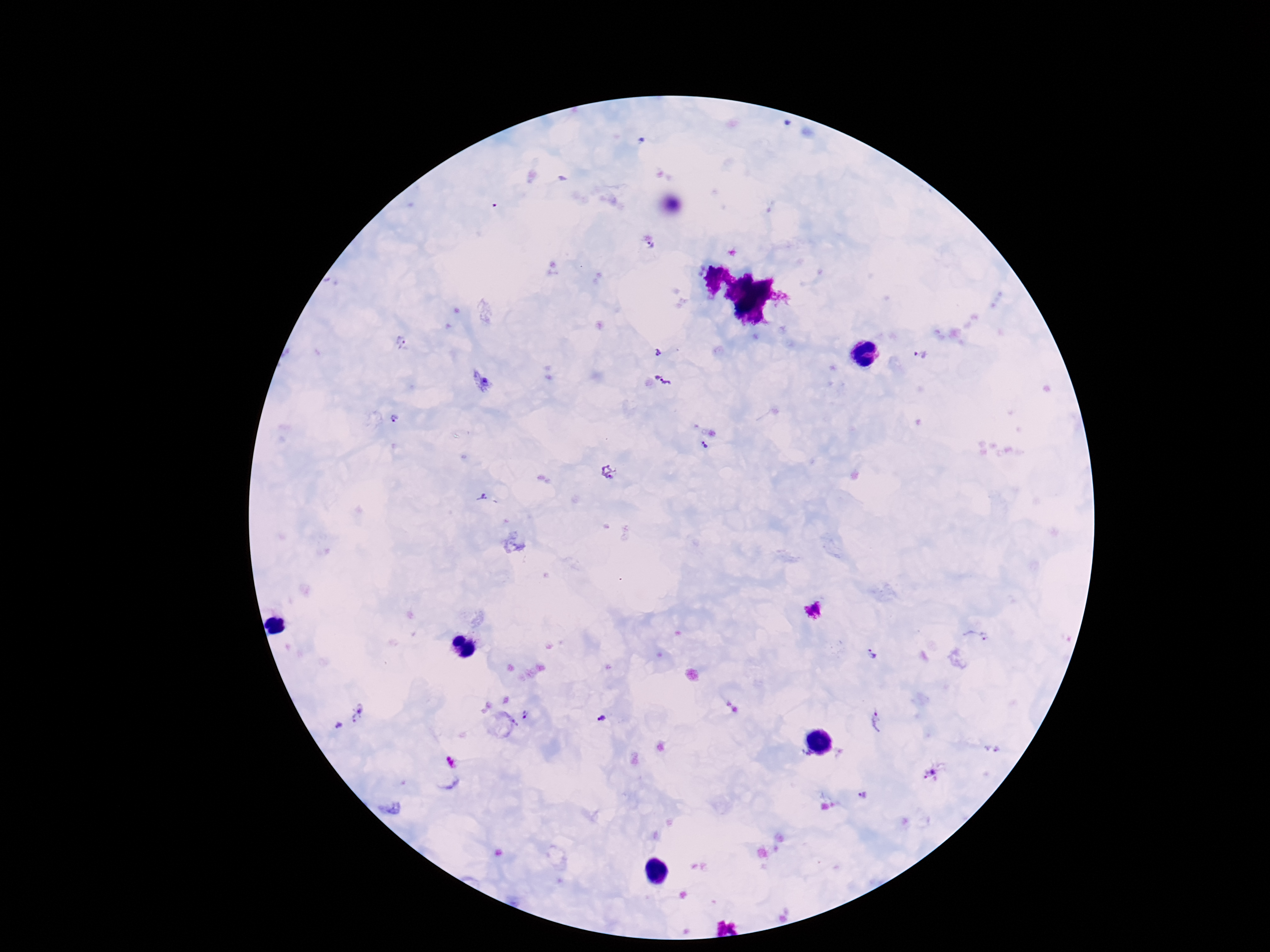 Approximate centers as [x, y] in pixels. Plasmodium parasite locations: [651, 246], [400, 341], [659, 352], [922, 356], [663, 381], [394, 419], [704, 445], [609, 472], [481, 498], [978, 635], [871, 654], [358, 712], [527, 716], [602, 719], [875, 720], [338, 726], [930, 774], [863, 793]. Smartphone photograph taken through the microscope eyepiece. Patient malaria status: infected. Single field of view. Thick blood film. 100x magnification. Image is 1270×952 pixels. Giemsa-stained preparation.